Locate every Plasmodium falciparum-infected red blood cell.
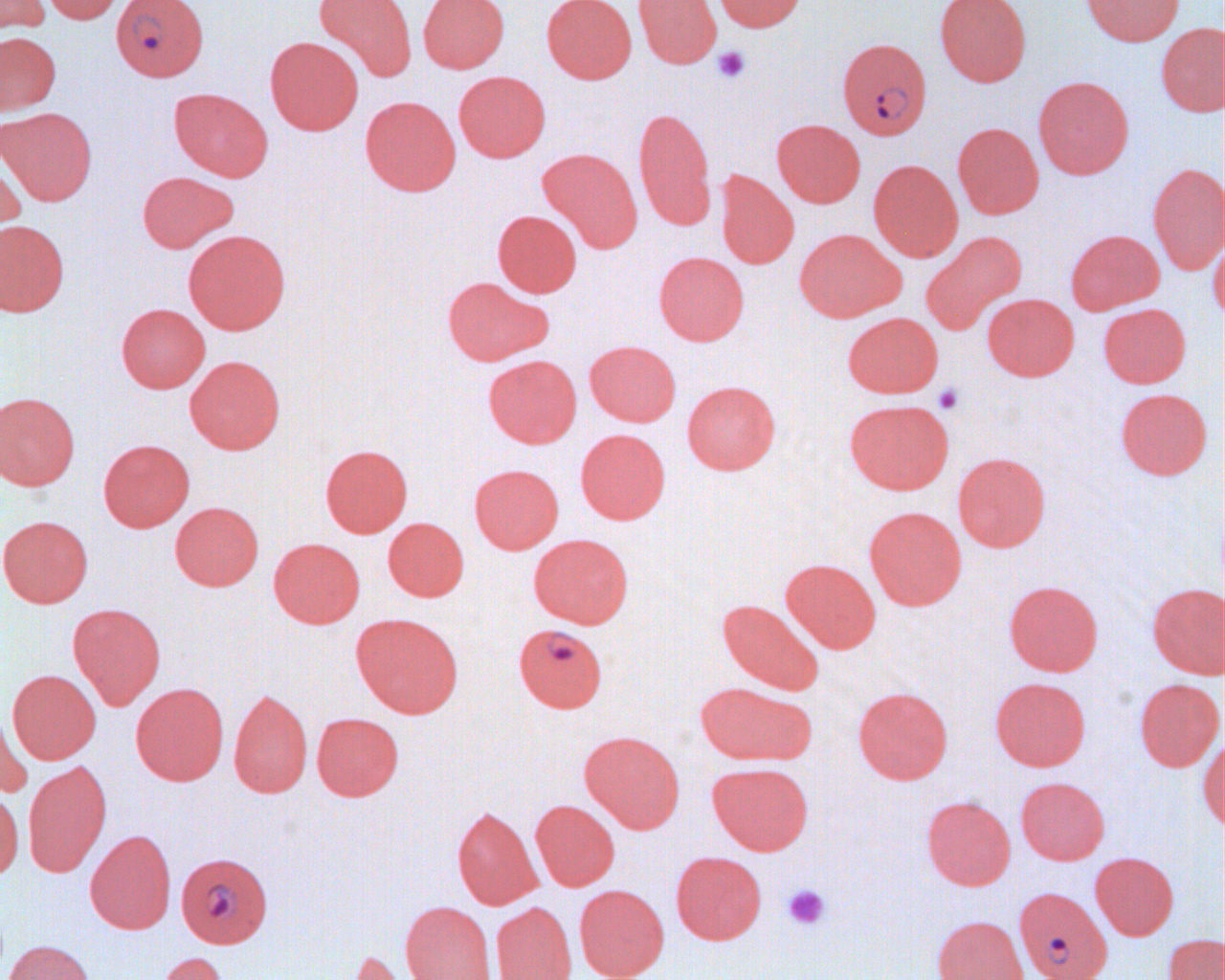

Approximate bounding boxes as (x1, y1, x2, y2) in pixels.
Plasmodium falciparum-infected red blood cells: (111, 0, 209, 81), (837, 38, 932, 139), (514, 623, 607, 712), (176, 857, 274, 950), (1014, 886, 1112, 980).

Uninfected red blood cell locations: (0, 0, 50, 35), (39, 0, 125, 24), (314, 0, 416, 83), (418, 0, 510, 73), (542, 0, 636, 83), (633, 0, 721, 68), (712, 0, 805, 32), (934, 0, 1032, 87), (1080, 0, 1184, 46), (1155, 23, 1224, 117), (0, 31, 61, 116), (265, 36, 363, 135), (454, 71, 550, 162), (1033, 75, 1134, 179), (169, 87, 273, 182), (360, 96, 461, 196), (633, 106, 717, 231), (1, 107, 98, 206), (772, 119, 866, 207), (952, 122, 1044, 219), (0, 148, 26, 249), (537, 148, 643, 254), (868, 159, 963, 262), (1148, 162, 1224, 276), (715, 170, 799, 269), (137, 171, 239, 253), (493, 210, 582, 297), (0, 220, 70, 317), (794, 228, 906, 322), (1065, 228, 1164, 315), (183, 229, 291, 335), (920, 230, 1027, 335), (1210, 237, 1224, 324), (654, 252, 749, 345), (442, 276, 551, 366), (982, 293, 1079, 381), (116, 303, 210, 392), (1098, 303, 1191, 388), (843, 312, 943, 398), (585, 341, 681, 426), (483, 354, 582, 448), (184, 355, 286, 454), (682, 380, 780, 474), (1115, 388, 1212, 480), (0, 391, 80, 490), (844, 399, 954, 494), (575, 428, 670, 524), (98, 439, 194, 532), (320, 444, 413, 537), (953, 452, 1051, 552), (469, 463, 564, 554), (170, 502, 264, 590), (864, 506, 967, 610), (0, 515, 93, 608), (383, 518, 469, 601), (528, 533, 634, 628), (269, 538, 364, 628), (780, 558, 881, 653), (1004, 580, 1103, 676), (1147, 583, 1223, 679), (718, 598, 825, 695), (67, 603, 166, 709), (351, 612, 464, 717), (8, 669, 101, 764), (990, 677, 1091, 771), (1135, 678, 1223, 772), (695, 681, 817, 765), (131, 682, 229, 785), (854, 686, 953, 784), (228, 688, 313, 798), (0, 704, 32, 798), (312, 712, 403, 801), (1200, 730, 1224, 833), (580, 731, 685, 833), (23, 760, 112, 877), (708, 762, 813, 855), (1015, 777, 1109, 864), (0, 789, 24, 881), (921, 795, 1016, 890), (530, 799, 619, 891), (452, 806, 541, 910), (85, 829, 176, 934), (671, 851, 767, 945), (1090, 851, 1179, 940), (574, 884, 669, 980), (400, 901, 497, 980), (491, 902, 577, 980), (931, 915, 1029, 980), (1162, 933, 1224, 980), (3, 939, 96, 980), (342, 948, 420, 980), (153, 951, 229, 980). Platelet locations: (712, 46, 750, 84), (933, 384, 964, 414), (781, 884, 830, 930). Slide-level diagnosis: Plasmodium falciparum. Single field of view. 1000x magnification. Optical microscopy. Thin blood smear. Image is 1225×980 pixels.